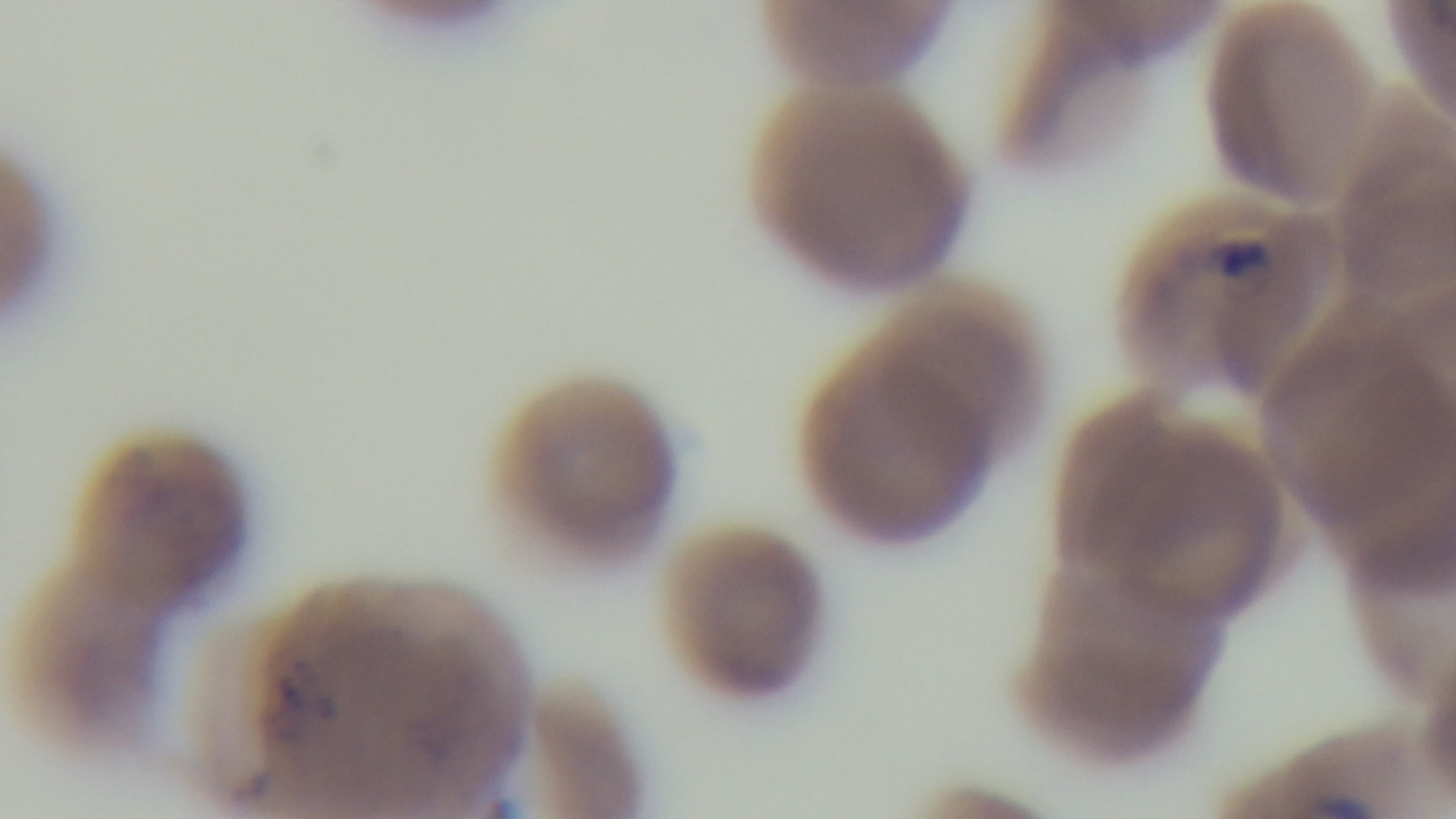
modality = light microscopy
objective = 100x oil immersion
stain = Giemsa
malaria status = positive
preparation = thin blood film
capture = mounted 4K digital camera
field of view = one from the slide